Name the cell type shown.
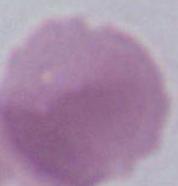
An erythrocyte.

modality = photomicrograph
magnification = 1000x